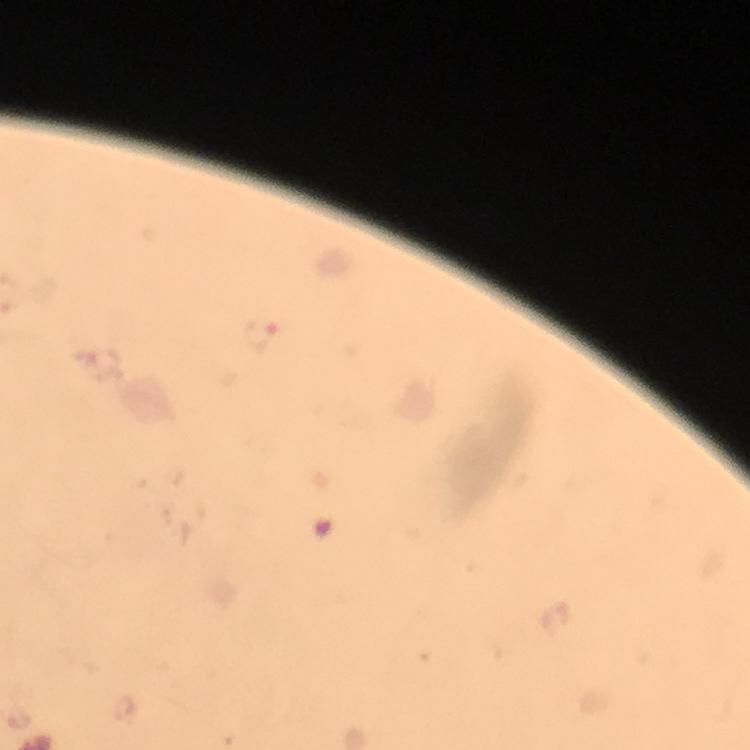
preparation: thick smear
stain: Giemsa
capture: smartphone photograph through a microscope
malaria_parasite_locations: 'approximate object centers, in pixels from the top-left corner: (x=260, y=337)'
cropped_from: a single field of view
image_size: 750×750 pixels
immersion_oil: applied
magnification: 100x
context: from a malaria diagnostic workup